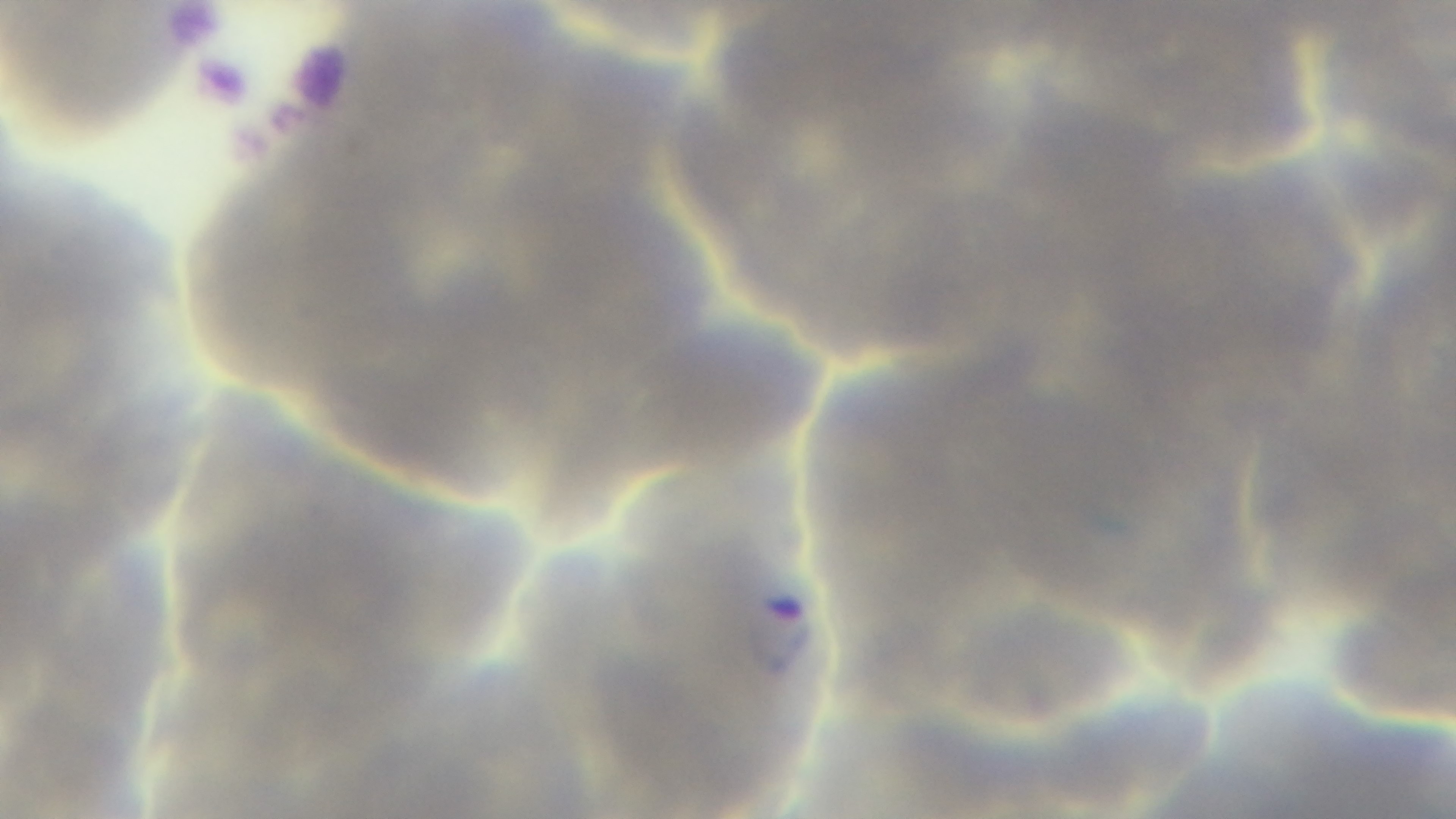
Summary:
  - Modality: light microscopy
  - Capture: mounted 4K digital camera
  - Field of view: single
  - Preparation: thin
  - Malaria status: positive
  - Stain: Giemsa
  - Objective: 100x oil immersion